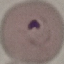
{
  "result": "malaria parasites identified",
  "image_type": "automatically extracted cell patch, resized to 64 × 64 pixels",
  "capture": "smartphone through the microscope eyepiece",
  "preparation": "thin blood film",
  "stain": "Giemsa"
}